State which parasite is depicted.
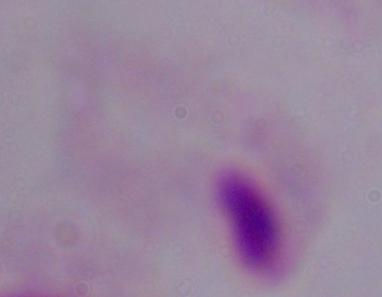

A trichomonad.

Captured at 1000x magnification. Photomicrograph.